Assess for Plasmodium parasites.
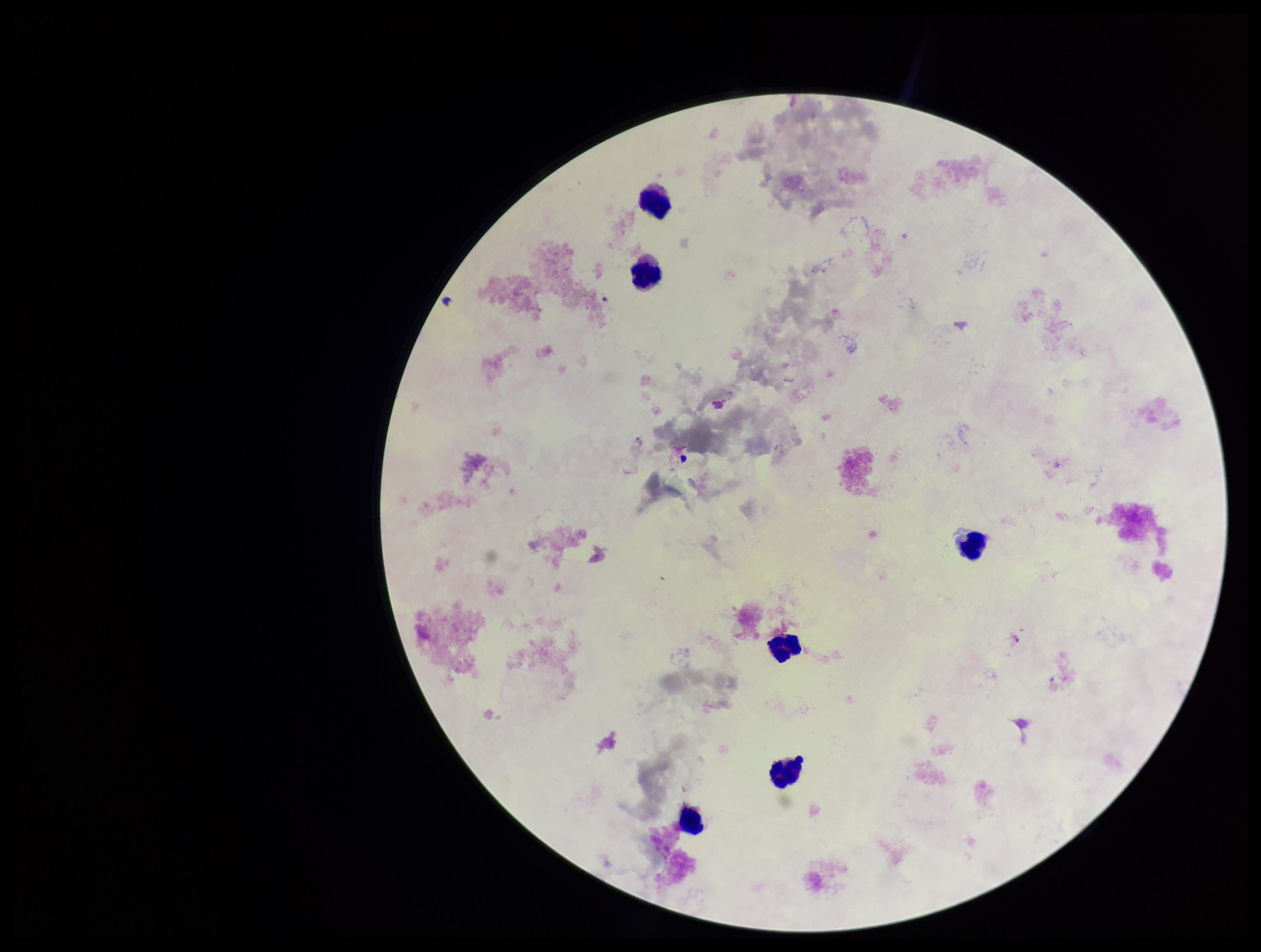
None identified.

Parasite count: 0. Patient malaria status: negative. Leukocyte count: 6. Image is 1261×952 pixels. Giemsa stain. Preparation: thick smear. Photographed through the microscope eyepiece with a smartphone camera. One field from this slide.